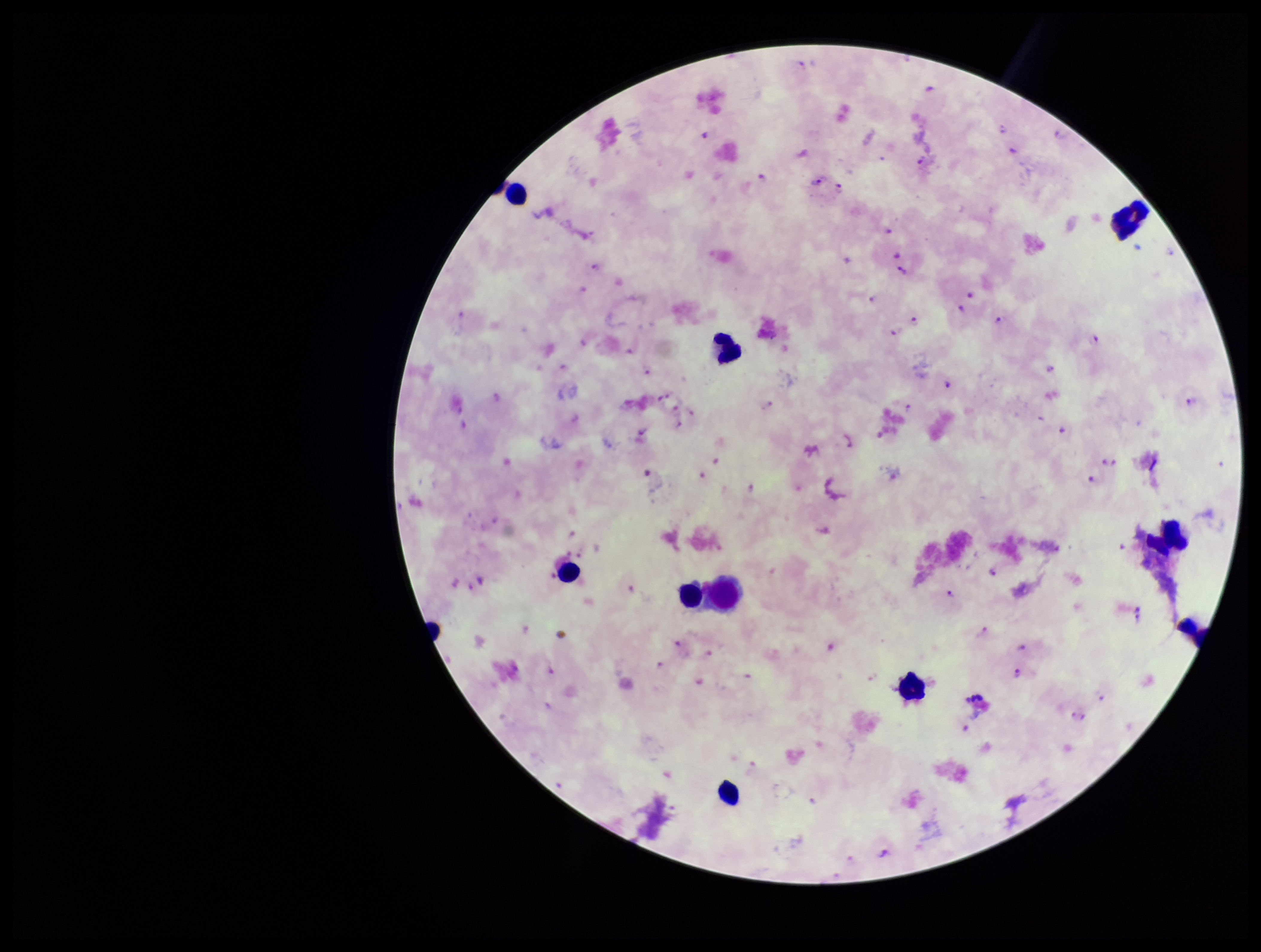
Parasite count: 69. Giemsa stain. Photographed through the microscope eyepiece with a smartphone camera. Species reported for this patient: Plasmodium falciparum. Preparation: thick blood smear. Plasmodium parasites: identified. Patient malaria status: positive. Leukocyte count: 9. Image is 1261×952 pixels. Single field of view.